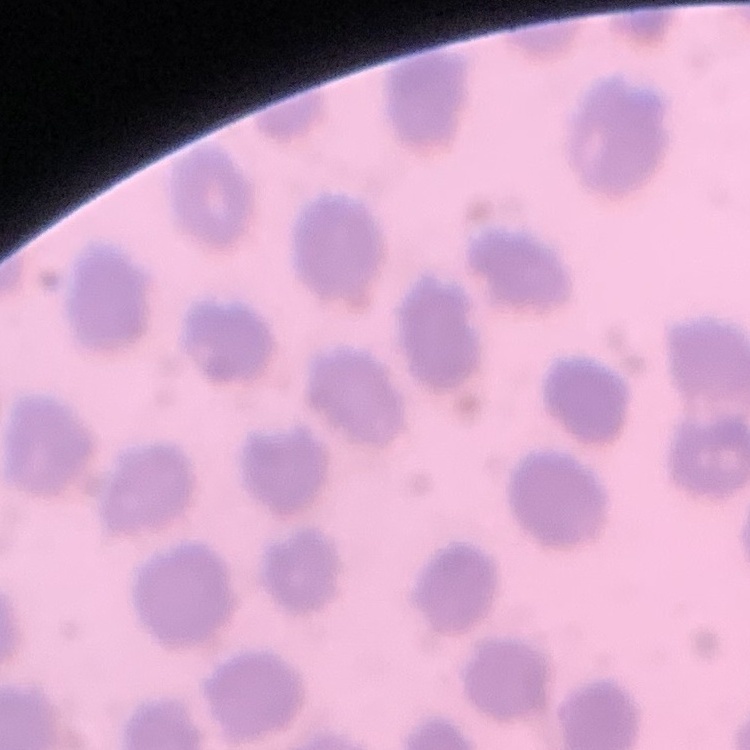
{
  "red_blood_cell_morphology": "no rouleaux formation",
  "stain": "Field's or Giemsa",
  "image_type": "square crop of a larger photomicrograph",
  "preparation": "thin blood smear"
}